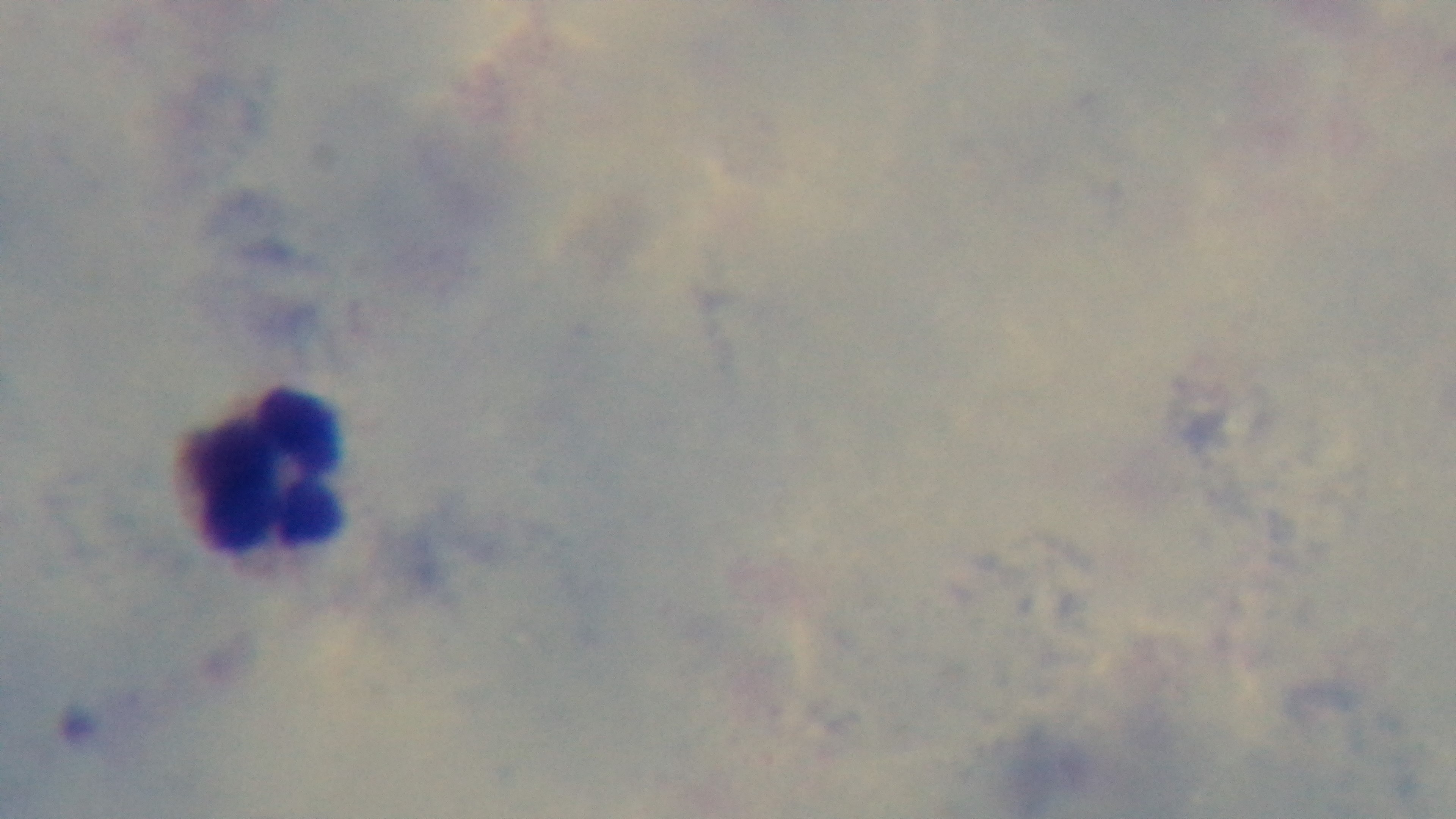

Summary:
  - Field of view: one from the slide
  - Objective: 100x oil immersion
  - Capture: mounted 4K digital camera
  - Malaria status: uninfected
  - Preparation: thick blood film
  - Modality: light microscopy
  - Stain: Giemsa